Comment on the morphology of the erythrocytes.
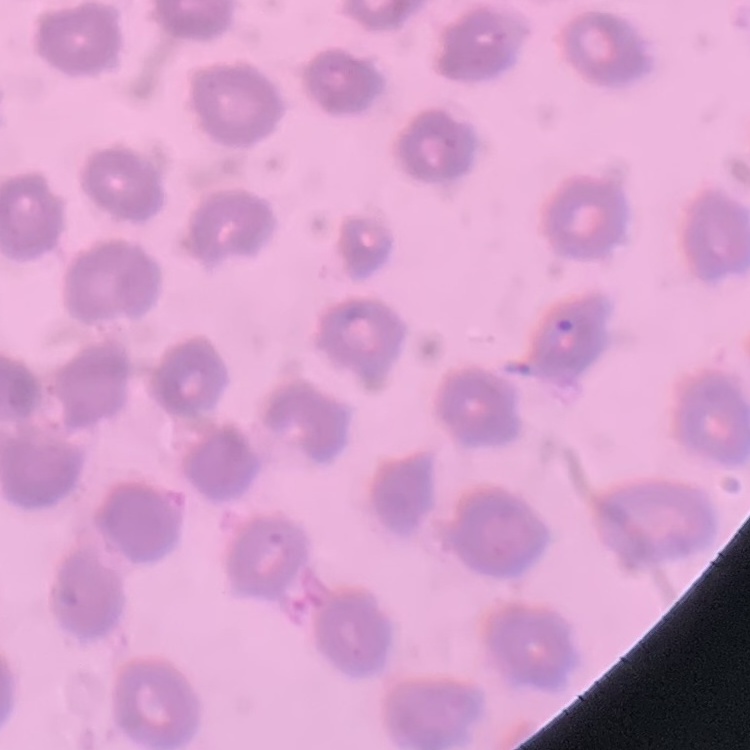

They show no rouleaux formation.

Square crop of a larger photomicrograph. Field's or Giemsa stain. Thin blood film.